Comment on the morphology of the erythrocytes.
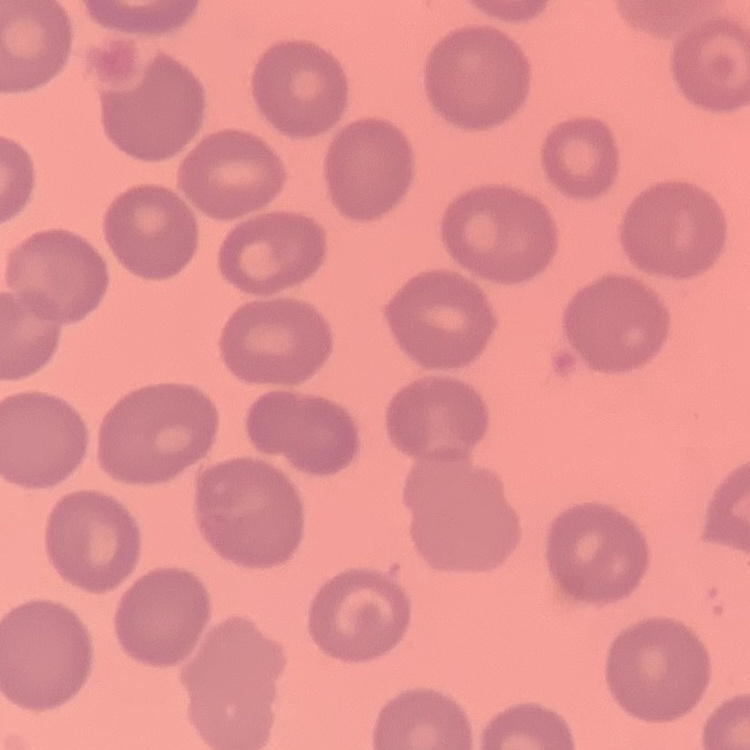
No rouleaux formation.

Summary:
  - Image type: square crop of a larger photomicrograph
  - Stain: Field's or Giemsa
  - Preparation: thin blood film